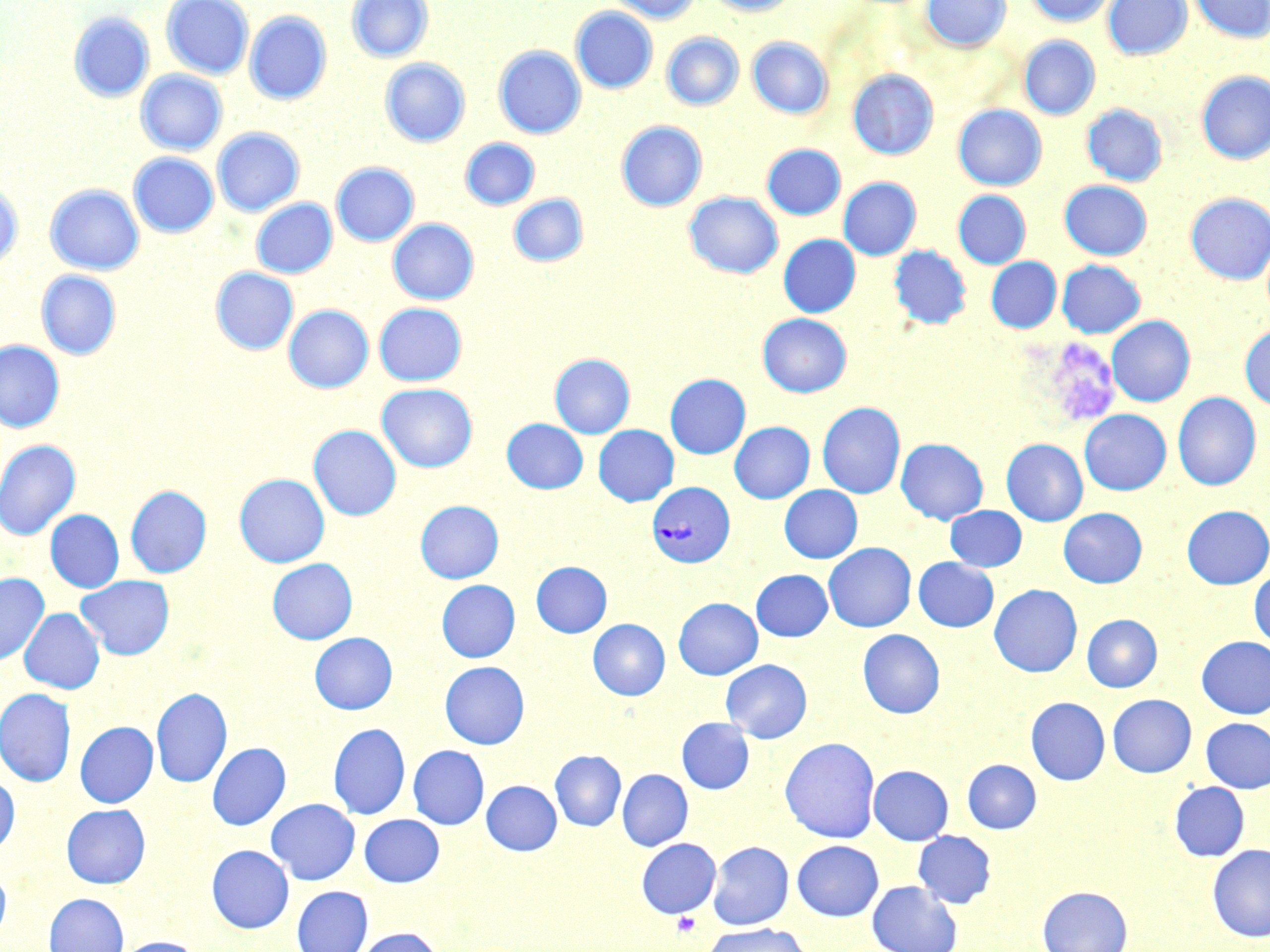
Summary:
  - Coordinate format: approximate bounding boxes as [x1, y1, x2, y2] in pixels
  - Uninfected red blood cell locations: [161, 0, 253, 79], [347, 0, 433, 63], [607, 0, 700, 24], [706, 0, 798, 16], [922, 0, 1010, 51], [1027, 0, 1115, 27], [1103, 0, 1192, 59], [1189, 0, 1269, 42], [570, 7, 657, 93], [245, 11, 331, 105], [68, 12, 154, 102], [662, 32, 744, 111], [1019, 36, 1100, 119], [747, 37, 832, 119], [494, 45, 586, 138], [380, 59, 469, 147], [848, 69, 939, 159], [136, 70, 227, 155], [1197, 70, 1270, 164], [953, 104, 1046, 190], [1082, 104, 1168, 186], [616, 121, 707, 211], [212, 127, 304, 216], [460, 138, 540, 210], [761, 144, 845, 220], [128, 153, 218, 238], [331, 162, 419, 246], [838, 177, 921, 260], [1059, 180, 1152, 260], [0, 184, 23, 271], [45, 185, 144, 275], [953, 190, 1031, 269], [684, 191, 783, 278], [1185, 192, 1270, 284], [508, 193, 588, 267], [251, 198, 336, 278], [388, 219, 479, 305], [779, 235, 860, 317], [888, 245, 971, 330], [986, 257, 1061, 333], [1056, 260, 1145, 338], [211, 267, 298, 355], [36, 270, 121, 359], [374, 302, 467, 386], [283, 305, 373, 392], [758, 313, 851, 397], [1107, 316, 1195, 406], [1240, 323, 1270, 411], [0, 340, 64, 432], [549, 354, 635, 438], [665, 373, 750, 459], [377, 383, 477, 472], [1172, 392, 1261, 491], [817, 401, 906, 498], [1079, 409, 1171, 495], [502, 419, 588, 493], [729, 421, 814, 503], [308, 425, 401, 520], [593, 425, 679, 506], [896, 438, 988, 524], [1002, 439, 1088, 526], [0, 440, 81, 541], [234, 473, 329, 567], [125, 485, 211, 578], [779, 485, 862, 563], [415, 500, 504, 583], [945, 505, 1027, 571], [1182, 505, 1270, 589], [1059, 507, 1147, 587], [45, 509, 124, 592], [824, 543, 916, 631], [914, 557, 998, 631], [267, 558, 357, 644], [531, 562, 611, 637], [751, 569, 832, 641], [1250, 570, 1270, 650], [0, 573, 49, 665], [75, 575, 174, 660], [437, 580, 519, 662], [989, 584, 1082, 677], [673, 597, 763, 679], [19, 608, 104, 694], [1082, 614, 1162, 692], [588, 619, 669, 700], [858, 629, 945, 718], [310, 632, 397, 714], [1197, 636, 1270, 718], [721, 659, 812, 743], [440, 661, 529, 749], [151, 687, 232, 788], [0, 689, 75, 786], [1107, 694, 1196, 777], [1026, 697, 1110, 784], [677, 718, 754, 794], [1201, 718, 1270, 792], [75, 721, 158, 807], [328, 723, 410, 820], [780, 736, 881, 843], [207, 742, 291, 830], [408, 745, 489, 829], [550, 750, 626, 831], [962, 759, 1042, 833], [869, 765, 953, 845], [618, 769, 692, 850], [0, 774, 19, 857], [482, 780, 561, 855], [1168, 781, 1249, 861], [266, 798, 360, 884], [61, 804, 150, 888], [360, 814, 444, 887], [913, 831, 996, 908], [636, 838, 721, 917], [792, 840, 884, 921], [708, 841, 794, 930], [1207, 844, 1270, 942], [206, 845, 293, 933], [0, 868, 10, 943], [868, 881, 962, 952], [1037, 885, 1132, 952], [292, 886, 373, 952], [44, 892, 128, 952], [702, 923, 810, 952], [354, 927, 445, 952], [116, 936, 203, 952]
  - Plasmodium vivax-infected red blood cell locations: [647, 482, 734, 567]
  - Platelet locations: [673, 912, 701, 939]
  - Slide-level diagnosis: Plasmodium vivax
  - Magnification: 1000x
  - Preparation: thin blood smear
  - Image size: 1270×952 pixels
  - Field of view: single
  - Stain: May-Grünwald-Giemsa
  - Modality: light microscopy